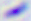

magnification = 400x
identification = Toxoplasma gondii
modality = micrograph